Identify the parasite.
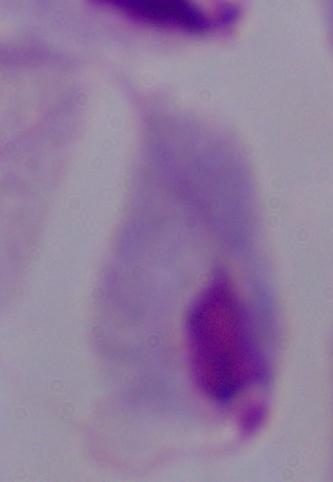

This is a trichomonad.

Photomicrograph. 1000x magnification.